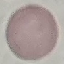
Result: no malaria parasites seen. Giemsa-stained preparation. Cell patch, automatically extracted from a larger field of view and resized to 64 × 64 pixels. Thin smear of blood. Photographed with a smartphone camera at the microscope eyepiece.